State which parasite is depicted.
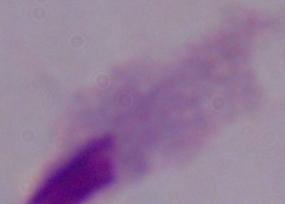
A trichomonad.

Summary:
  - Modality: photomicrograph
  - Magnification: 1000x